Identify the parasite.
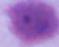

This is Plasmodium.

Micrograph. 400x or 1000x magnification.